Name the parasite shown.
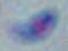

This is Toxoplasma gondii.

1000x magnification. Photomicrograph.